Point out each leukocyte.
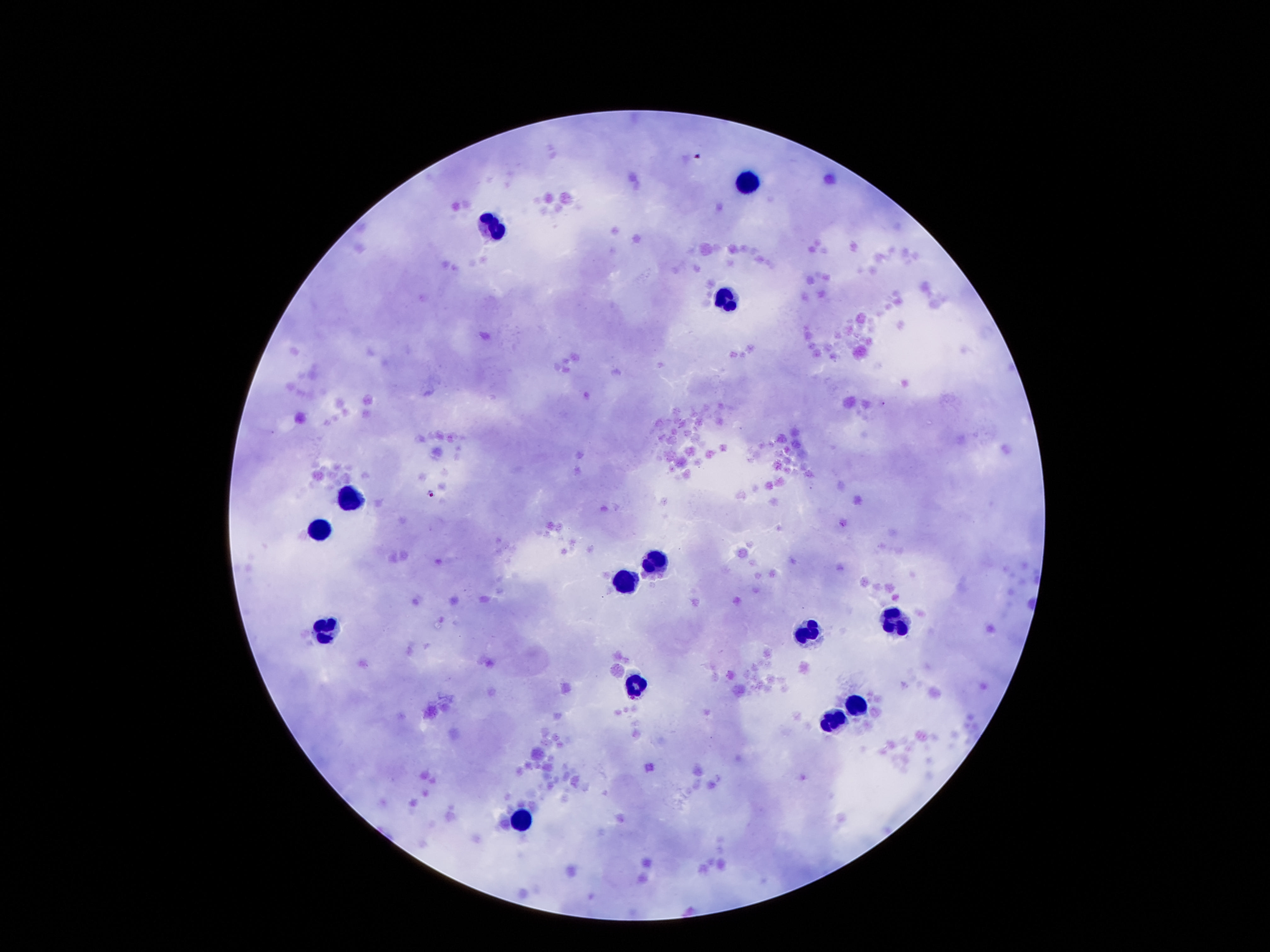
Approximate centers as {x, y} in pixels.
Leukocytes: {745, 183}, {493, 228}, {726, 299}, {348, 501}, {318, 534}, {648, 568}, {629, 583}, {896, 620}, {327, 627}, {808, 631}, {636, 686}, {856, 705}, {835, 723}, {520, 818}.

magnification = 100x
capture = smartphone camera through the microscope eyepiece
field of view = single
image size = 1270×952 pixels
patient malaria status = negative
preparation = thick peripheral-blood smear
stain = Giemsa